Assess this cell for malaria.
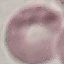

It is uninfected.

Automatically extracted cell patch, resized to 64 × 64 pixels. Photographed with a smartphone camera at the microscope eyepiece. Thin blood film. Giemsa-stained preparation.